Assess this cell for malaria.
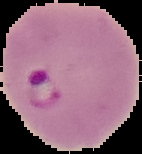
It is parasitized.

Cell region segmented out of the field of view; the surrounding area is masked to black. From a thin blood film. Image is 142×154 pixels.